Report the malaria status of this cell.
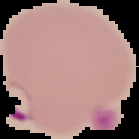
Parasitized.

Summary:
  - Preparation: thin blood smear
  - Image size: 139×139 pixels
  - Image type: cell region segmented out of the field of view; surrounding area masked to black